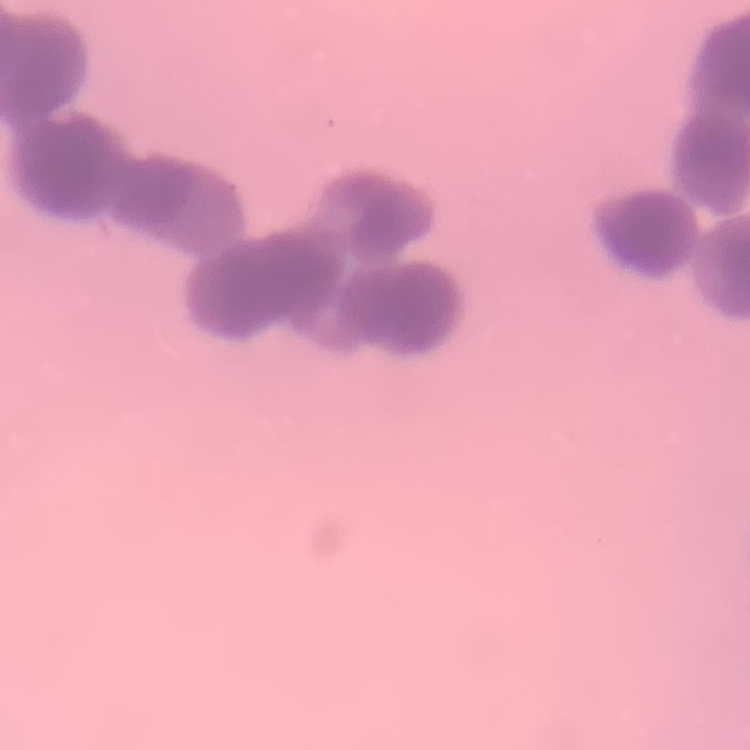
The erythrocytes show rouleaux formation. Square crop of a larger photomicrograph. Thin blood film. Stained with either Field's or Giemsa.